Which red blood cells are P. falciparum-infected, and which are of indeterminate infection status?
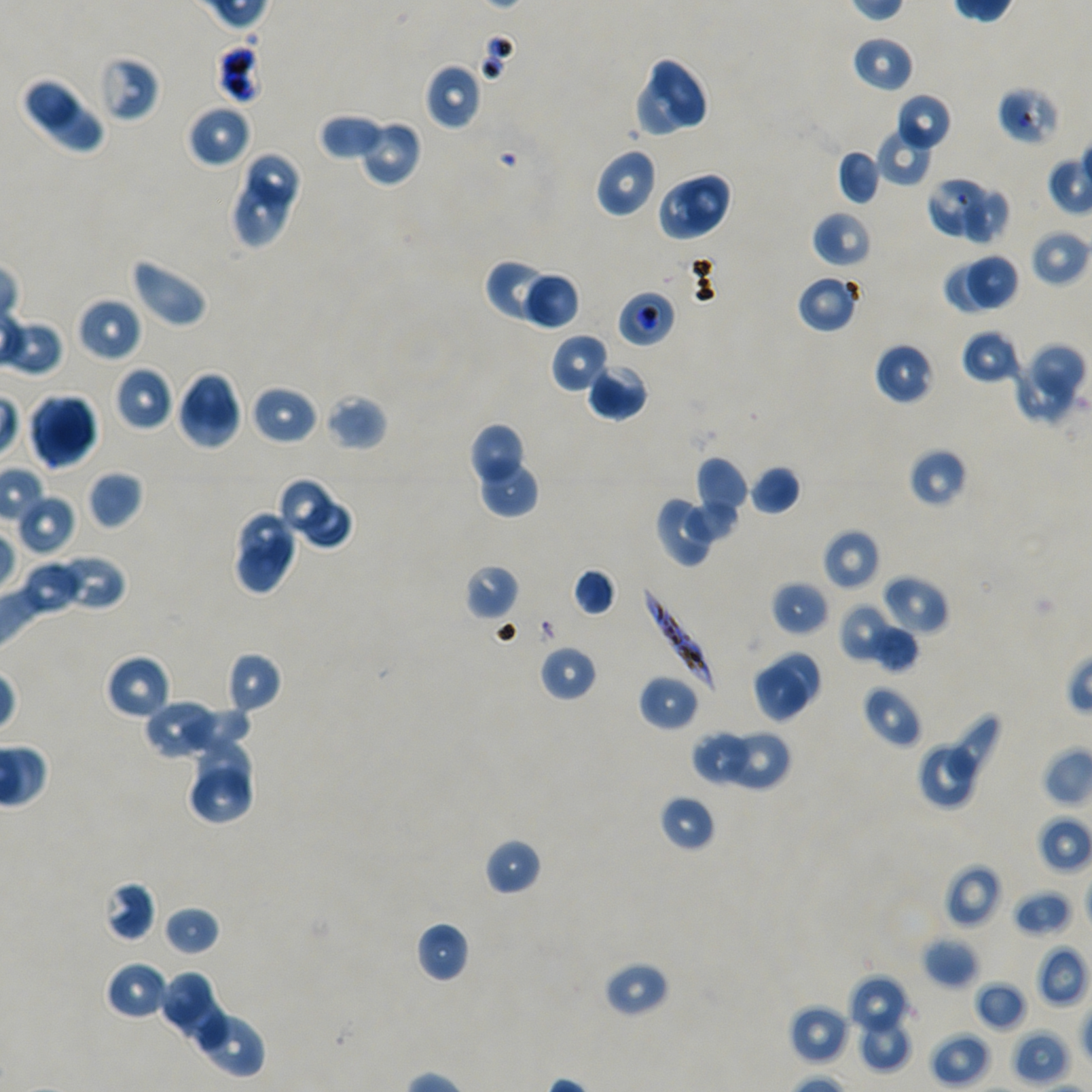

Approximate bounding boxes as [x1, y1, x2, y2] in pixels. Not every red blood cell is marked. A life-cycle stage — or a range of stages, where the recorded stages span more than one — follows each staged infected red blood cell.
Infected red blood cells: [617, 289, 677, 348] trophozoite; [642, 586, 716, 687].
Red blood cells of indeterminate infection status: [216, 41, 263, 104], [96, 54, 160, 122], [996, 86, 1060, 147].

Summary:
  - Locations of uninfected red blood cells: [851, 35, 915, 93], [651, 56, 706, 129], [424, 62, 483, 130], [20, 75, 87, 136], [632, 77, 691, 136], [895, 93, 952, 152], [46, 101, 103, 151], [186, 104, 251, 168], [318, 113, 386, 161], [362, 124, 420, 184], [877, 127, 934, 187], [594, 147, 658, 218], [837, 149, 881, 205], [248, 151, 299, 211], [677, 170, 734, 234], [926, 176, 986, 235], [236, 177, 290, 249], [657, 183, 722, 241], [962, 189, 1006, 243], [812, 210, 873, 268], [1030, 228, 1091, 287], [967, 252, 1017, 310], [130, 257, 209, 328], [943, 261, 1000, 314], [484, 263, 562, 323], [527, 272, 581, 330], [796, 273, 860, 333], [76, 297, 142, 363], [961, 329, 1021, 385], [551, 333, 611, 394], [874, 342, 935, 405], [1033, 344, 1085, 400], [586, 362, 649, 421], [113, 365, 175, 431], [1017, 365, 1072, 420], [176, 371, 242, 450], [250, 384, 318, 445], [323, 393, 388, 452], [29, 394, 98, 469], [469, 421, 523, 480], [908, 448, 968, 508], [477, 456, 541, 517], [694, 456, 749, 528], [748, 464, 801, 515], [87, 469, 143, 530], [276, 475, 334, 532], [17, 494, 75, 555], [302, 498, 354, 549], [655, 498, 711, 568], [687, 498, 738, 541], [239, 511, 295, 562], [822, 529, 881, 591], [236, 534, 299, 596], [52, 553, 126, 612], [19, 561, 84, 614], [463, 564, 520, 621], [572, 567, 617, 617], [881, 574, 949, 636], [770, 580, 831, 636], [837, 602, 894, 664], [869, 625, 919, 672], [539, 644, 598, 703], [225, 651, 283, 715], [770, 652, 820, 708], [105, 654, 171, 720], [751, 663, 810, 723], [638, 674, 700, 731], [861, 683, 923, 748], [143, 698, 216, 759], [179, 703, 252, 750], [947, 714, 1001, 780], [693, 727, 747, 786], [726, 733, 789, 789], [194, 738, 252, 794], [917, 743, 977, 811], [193, 767, 251, 821], [658, 793, 716, 852], [1038, 814, 1092, 873], [484, 837, 543, 896], [944, 863, 1002, 929], [103, 880, 156, 942], [1012, 888, 1074, 938], [162, 905, 221, 956], [415, 921, 471, 983], [922, 936, 980, 989], [1035, 944, 1089, 1008], [604, 960, 670, 1018], [105, 961, 170, 1021], [159, 970, 212, 1026], [848, 975, 911, 1037], [973, 980, 1027, 1032], [173, 996, 230, 1049], [788, 1004, 852, 1067], [196, 1013, 266, 1079], [858, 1014, 913, 1072], [928, 1030, 991, 1089], [1010, 1030, 1072, 1087]
  - Field of view: single
  - Donor blood group: A+/O+
  - Culture: static in-vitro P. falciparum strain NF54
  - Image size: 1092×1092 pixels
  - Preparation: thin blood smear
  - Objective: 100x, oil immersion, numerical aperture 1.45
  - Stain: Giemsa